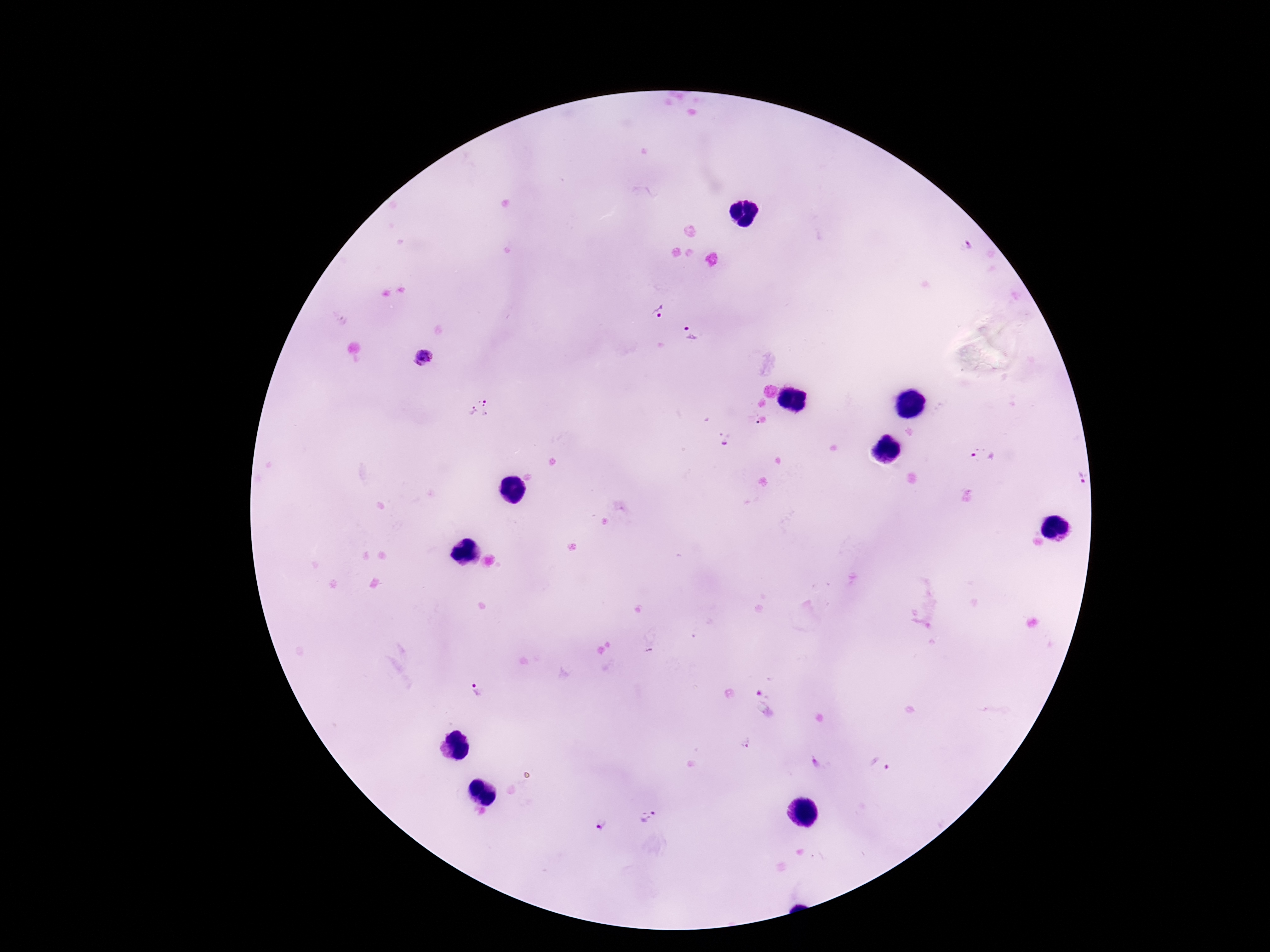
Approximate centers as {x, y} in pixels.
Summary:
  - Plasmodium parasite locations: {965, 244}, {658, 310}, {694, 333}, {423, 358}, {481, 408}, {723, 439}, {984, 458}, {1082, 478}, {475, 694}, {764, 702}, {744, 741}, {814, 762}, {878, 764}, {648, 818}, {601, 825}
  - Magnification: 100x
  - Capture: smartphone camera through the microscope eyepiece
  - Patient malaria status: positive
  - Preparation: thick blood film
  - Stain: Giemsa
  - Field of view: single
  - Image size: 1270×952 pixels